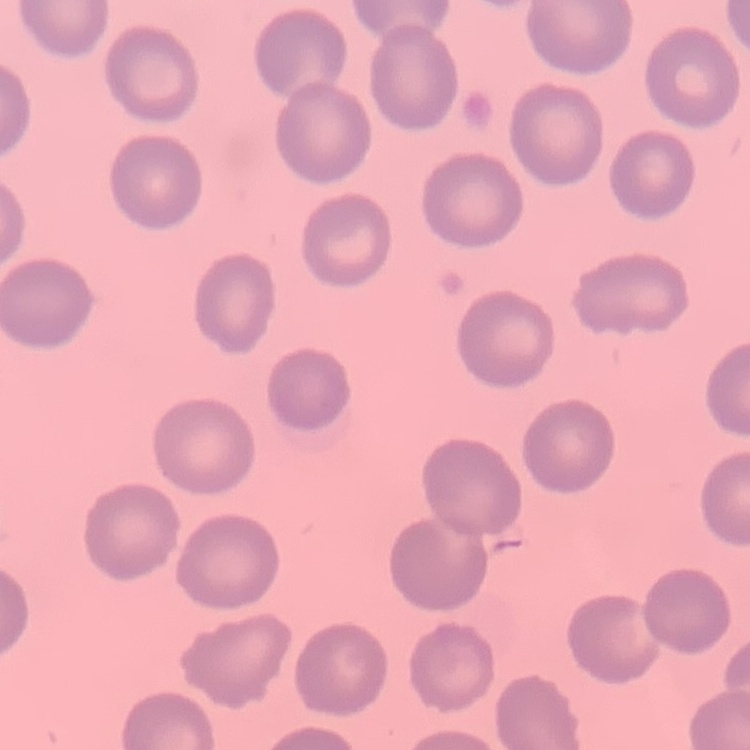
Summary:
  - Erythrocyte morphology: no rouleaux formation
  - Stain: Field's or Giemsa
  - Preparation: thin blood film
  - Image type: square crop of a larger photomicrograph